Assess this cell for malaria.
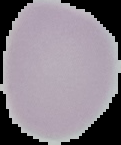
Uninfected.

preparation = thin blood smear
image type = segmented cell region with the area outside set to black
image size = 121×145 pixels